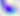

modality = micrograph
magnification = 400x
identification = Toxoplasma gondii